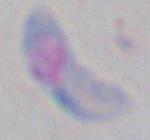
modality = photomicrograph
magnification = 1000x
identification = Toxoplasma gondii